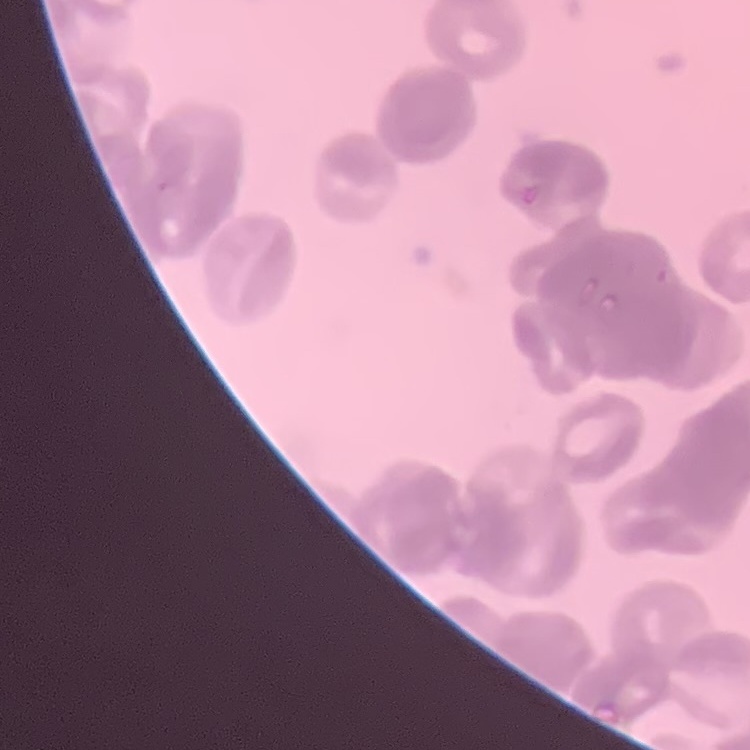

The erythrocytes show rouleaux formation. Thin blood smear. Square crop of a larger photomicrograph. Stained with either Field's or Giemsa.